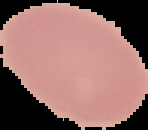
Summary:
  - Image type: segmented cell region on a black background
  - Preparation: thin blood film
  - Image size: 148×130 pixels
  - Malaria status: uninfected